Give the position of every malaria parasite and every leukocyte.
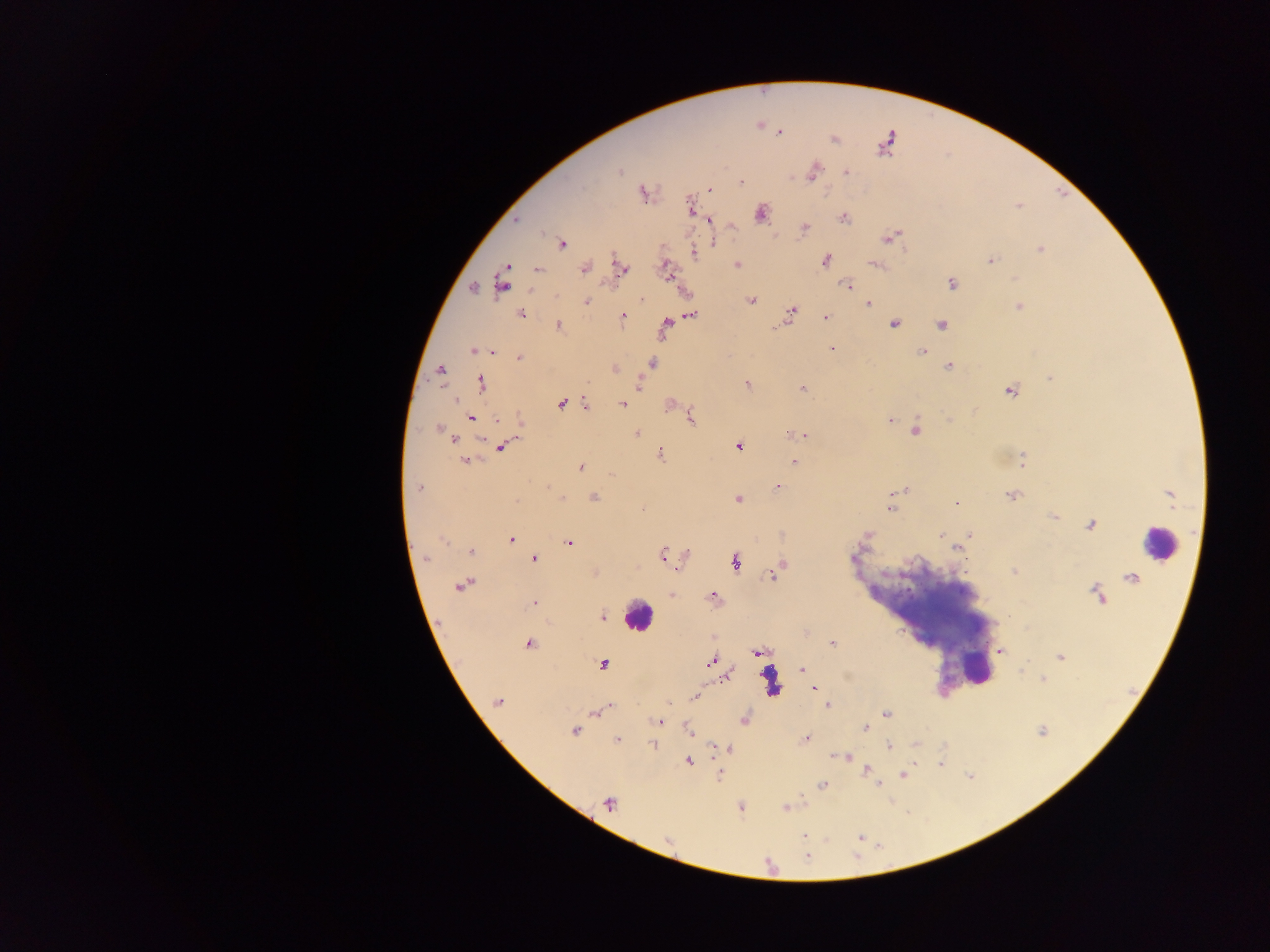
Approximate centers as {x, y} in pixels.
Malaria parasites: {758, 124}, {780, 131}, {834, 139}, {620, 171}, {812, 171}, {845, 172}, {741, 182}, {709, 190}, {642, 192}, {1018, 205}, {690, 206}, {761, 212}, {843, 217}, {710, 219}, {730, 224}, {805, 228}, {889, 237}, {711, 241}, {561, 242}, {1041, 249}, {692, 253}, {825, 260}, {990, 261}, {735, 264}, {876, 264}, {621, 268}, {665, 268}, {537, 269}, {584, 269}, {1014, 279}, {503, 280}, {951, 284}, {846, 285}, {473, 288}, {641, 298}, {751, 300}, {586, 301}, {868, 303}, {1019, 306}, {791, 312}, {521, 314}, {690, 314}, {621, 316}, {825, 317}, {893, 322}, {666, 324}, {941, 324}, {557, 325}, {831, 348}, {474, 350}, {490, 351}, {923, 352}, {520, 358}, {651, 363}, {948, 366}, {615, 368}, {440, 370}, {1050, 377}, {480, 383}, {637, 384}, {747, 384}, {803, 388}, {1010, 389}, {454, 400}, {561, 403}, {669, 403}, {586, 404}, {621, 404}, {471, 417}, {691, 418}, {889, 420}, {519, 421}, {438, 428}, {916, 430}, {636, 433}, {804, 435}, {793, 436}, {455, 438}, {502, 445}, {738, 446}, {659, 454}, {464, 459}, {1022, 460}, {794, 462}, {580, 466}, {610, 474}, {777, 485}, {418, 487}, {905, 490}, {1169, 494}, {1012, 495}, {561, 497}, {593, 497}, {737, 499}, {955, 502}, {890, 508}, {642, 510}, {1053, 516}, {1090, 525}, {941, 534}, {970, 534}, {442, 538}, {510, 539}, {568, 542}, {957, 547}, {471, 551}, {662, 555}, {683, 556}, {426, 558}, {533, 559}, {735, 561}, {776, 570}, {1013, 571}, {595, 573}, {1131, 577}, {463, 586}, {672, 595}, {1097, 595}, {713, 597}, {534, 602}, {602, 617}, {806, 632}, {528, 644}, {832, 644}, {1000, 650}, {758, 652}, {1060, 656}, {710, 662}, {602, 664}, {803, 670}, {725, 677}, {1043, 678}, {815, 688}, {694, 697}, {498, 701}, {610, 705}, {828, 705}, {606, 707}, {596, 711}, {886, 714}, {743, 718}, {660, 722}, {867, 727}, {689, 730}, {575, 731}, {1042, 731}, {805, 739}, {616, 740}, {653, 744}, {915, 744}, {889, 746}, {729, 748}, {835, 756}, {845, 756}, {687, 761}, {941, 764}, {867, 769}, {719, 774}, {902, 774}, {879, 784}, {822, 785}, {608, 804}, {740, 807}, {786, 807}, {860, 835}, {805, 836}, {668, 841}.
Leukocytes: {1161, 544}, {638, 615}, {978, 671}, {770, 684}.

Summary:
  - Country: Ghana
  - Preparation: thick blood smear
  - Capture: mobile-phone photograph through a microscope
  - Image size: 1270×952 pixels
  - Field of view: single